State which parasite is depicted.
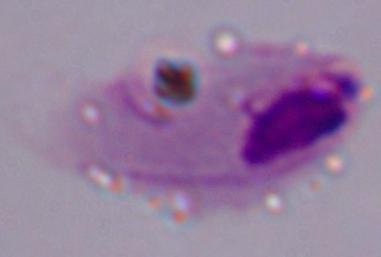

A trichomonad.

Photomicrograph. Captured at 1000x magnification.